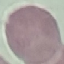 Malaria status: uninfected. Photographed with a smartphone camera at the microscope eyepiece. Giemsa-stained preparation. Thin blood film. Automatically extracted cell patch, resized to 64 × 64 pixels.